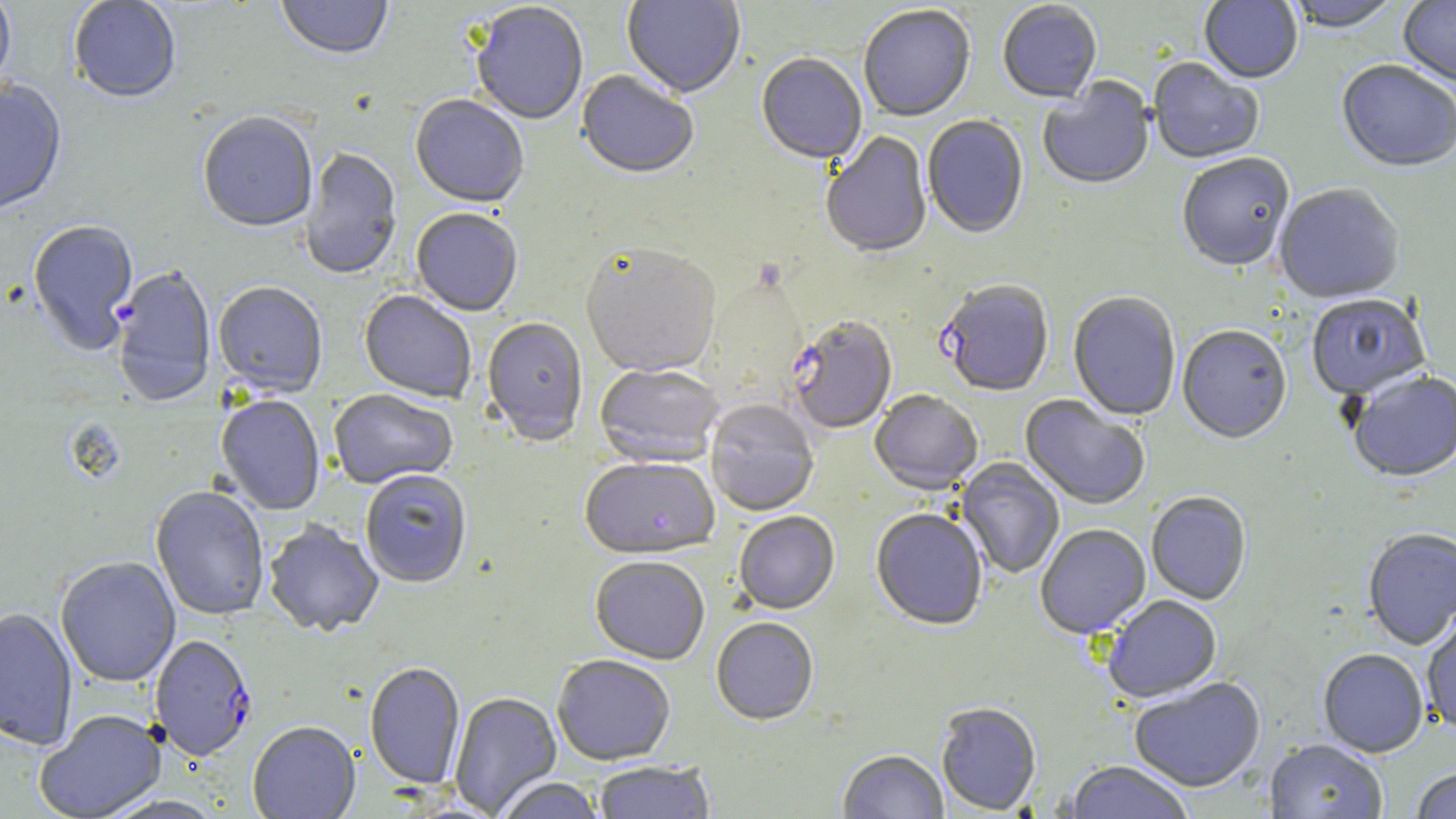

Summary:
  - Coordinate format: approximate bounding boxes as [x1, y1, x2, y2] in pixels
  - Uninfected red blood cell locations: [0, 0, 16, 94], [68, 0, 181, 105], [275, 0, 393, 62], [621, 0, 746, 100], [1199, 0, 1303, 86], [1283, 0, 1404, 35], [1398, 0, 1456, 89], [997, 2, 1103, 105], [470, 3, 588, 127], [859, 6, 976, 124], [755, 55, 867, 167], [1148, 59, 1264, 166], [1336, 62, 1456, 175], [576, 72, 699, 182], [1038, 79, 1155, 192], [0, 82, 67, 218], [410, 96, 529, 210], [197, 114, 318, 234], [921, 116, 1029, 241], [821, 132, 932, 261], [300, 147, 402, 281], [1176, 155, 1295, 274], [1274, 185, 1404, 305], [410, 210, 523, 318], [27, 221, 139, 357], [580, 246, 721, 380], [213, 283, 327, 398], [358, 291, 476, 404], [1068, 293, 1181, 422], [1305, 295, 1432, 402], [481, 318, 588, 448], [1177, 327, 1291, 446], [594, 365, 724, 469], [1348, 373, 1456, 484], [329, 390, 457, 491], [869, 392, 983, 497], [215, 396, 325, 516], [1019, 396, 1150, 510], [705, 401, 819, 517], [955, 458, 1065, 579], [580, 459, 719, 562], [360, 472, 472, 589], [151, 487, 270, 622], [1146, 493, 1251, 605], [871, 510, 987, 633], [734, 512, 840, 616], [264, 521, 384, 638], [1036, 525, 1151, 640], [1363, 529, 1456, 650], [55, 557, 181, 688], [590, 559, 710, 666], [1103, 596, 1222, 704], [0, 608, 78, 752], [1422, 608, 1456, 736], [711, 619, 819, 728], [1318, 650, 1429, 759], [552, 657, 675, 767], [365, 663, 465, 790], [1129, 678, 1267, 793], [448, 693, 563, 817], [936, 705, 1041, 816], [34, 711, 167, 819], [247, 724, 361, 819], [1265, 740, 1387, 819], [837, 751, 948, 819], [593, 761, 715, 818], [1062, 762, 1195, 819], [1410, 769, 1456, 819], [493, 778, 606, 819]
  - Plasmodium falciparum-infected red blood cell locations: [112, 266, 217, 409], [938, 281, 1055, 399], [788, 318, 897, 436], [150, 636, 257, 762]
  - Slide-level diagnosis: Plasmodium falciparum
  - Preparation: thin blood film
  - Image size: 1456×819 pixels
  - Magnification: 1000x
  - Stain: May-Grünwald-Giemsa
  - Modality: optical microscopy
  - Field of view: single